Identify the parasite.
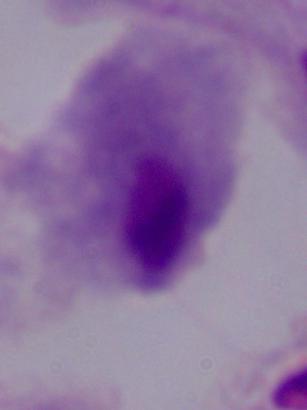

This is a trichomonad.

Summary:
  - Modality: micrograph
  - Magnification: 1000x